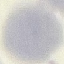
Summary:
  - Malaria status: uninfected
  - Capture: smartphone through the microscope eyepiece
  - Image type: automatically extracted cell patch, resized to 64 × 64 pixels
  - Preparation: thin blood smear
  - Stain: Giemsa